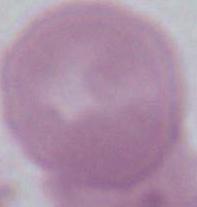
magnification = 1000x
modality = micrograph
identification = erythrocyte